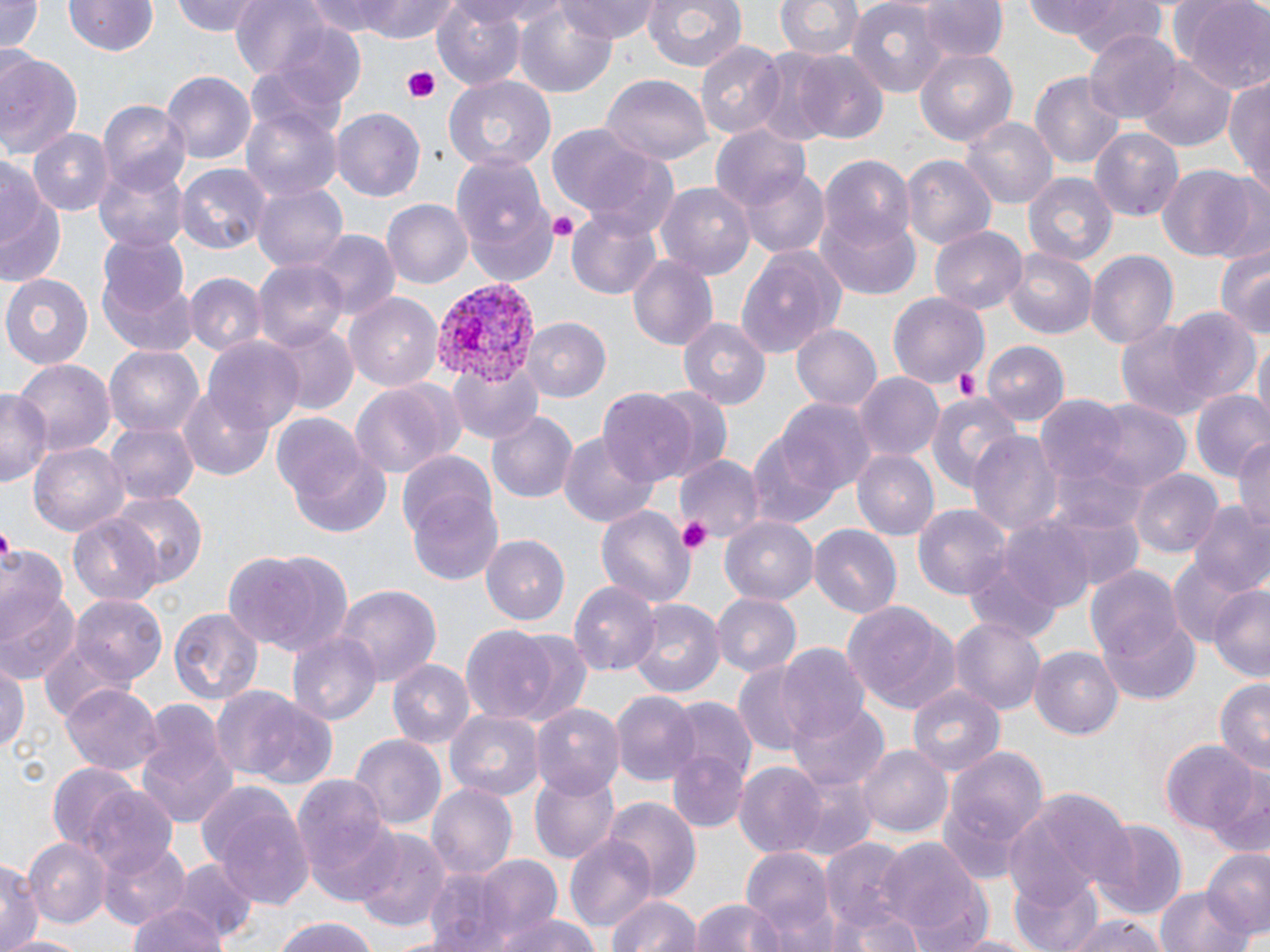

{
  "slide_level_diagnosis": "Plasmodium vivax",
  "preparation": "thin blood film",
  "platelet_locations": "approximate bounding boxes as named x1/y1/x2/y2 corners in pixels: (x1=401, y1=64, x2=444, y2=107), (x1=546, y1=211, x2=578, y2=239), (x1=951, y1=366, x2=983, y2=399), (x1=678, y1=517, x2=714, y2=556), (x1=0, y1=530, x2=17, y2=561)",
  "image_size": "1270×952 pixels",
  "field_of_view": "one of a larger specimen",
  "magnification": "1000x",
  "plasmodium_vivax_infected_red_blood_cell_locations": "approximate bounding boxes as named x1/y1/x2/y2 corners in pixels: (x1=430, y1=283, x2=538, y2=390)",
  "uninfected_red_blood_cell_locations": "approximate bounding boxes as named x1/y1/x2/y2 corners in pixels: (x1=0, y1=0, x2=43, y2=54), (x1=66, y1=0, x2=158, y2=58), (x1=172, y1=0, x2=265, y2=36), (x1=230, y1=0, x2=331, y2=79), (x1=305, y1=0, x2=402, y2=37), (x1=357, y1=0, x2=463, y2=41), (x1=430, y1=0, x2=529, y2=88), (x1=557, y1=0, x2=662, y2=42), (x1=642, y1=0, x2=748, y2=72), (x1=775, y1=0, x2=863, y2=62), (x1=847, y1=0, x2=948, y2=97), (x1=1025, y1=0, x2=1169, y2=52), (x1=1170, y1=0, x2=1270, y2=92), (x1=514, y1=1, x2=616, y2=97), (x1=917, y1=1, x2=1007, y2=64), (x1=1084, y1=28, x2=1183, y2=124), (x1=694, y1=41, x2=785, y2=143), (x1=914, y1=48, x2=1018, y2=145), (x1=0, y1=51, x2=85, y2=165), (x1=793, y1=52, x2=889, y2=144), (x1=1139, y1=60, x2=1233, y2=152), (x1=162, y1=70, x2=255, y2=162), (x1=1030, y1=71, x2=1127, y2=167), (x1=443, y1=76, x2=556, y2=173), (x1=601, y1=76, x2=711, y2=166), (x1=1226, y1=76, x2=1270, y2=188), (x1=100, y1=102, x2=193, y2=196), (x1=242, y1=102, x2=342, y2=204), (x1=331, y1=107, x2=425, y2=202), (x1=959, y1=116, x2=1057, y2=210), (x1=709, y1=123, x2=810, y2=216), (x1=545, y1=125, x2=670, y2=221), (x1=1089, y1=127, x2=1184, y2=221), (x1=27, y1=128, x2=112, y2=216), (x1=0, y1=150, x2=59, y2=275), (x1=450, y1=151, x2=557, y2=286), (x1=901, y1=155, x2=996, y2=252), (x1=820, y1=156, x2=916, y2=253), (x1=93, y1=159, x2=189, y2=249), (x1=1156, y1=163, x2=1263, y2=262), (x1=175, y1=164, x2=270, y2=256), (x1=741, y1=166, x2=831, y2=259), (x1=1024, y1=173, x2=1116, y2=264), (x1=658, y1=183, x2=755, y2=281), (x1=253, y1=184, x2=349, y2=274), (x1=383, y1=199, x2=472, y2=290), (x1=565, y1=206, x2=664, y2=300), (x1=818, y1=212, x2=921, y2=298), (x1=929, y1=225, x2=1028, y2=312), (x1=310, y1=231, x2=399, y2=321), (x1=97, y1=234, x2=191, y2=321), (x1=736, y1=246, x2=845, y2=358), (x1=1216, y1=247, x2=1270, y2=340), (x1=1005, y1=249, x2=1097, y2=340), (x1=1086, y1=250, x2=1177, y2=348), (x1=628, y1=252, x2=720, y2=351), (x1=253, y1=259, x2=349, y2=353), (x1=99, y1=271, x2=199, y2=360), (x1=2, y1=272, x2=95, y2=368), (x1=185, y1=272, x2=265, y2=357), (x1=346, y1=292, x2=444, y2=391), (x1=889, y1=293, x2=989, y2=387), (x1=1167, y1=310, x2=1260, y2=407), (x1=1113, y1=316, x2=1226, y2=419), (x1=522, y1=318, x2=611, y2=402), (x1=678, y1=318, x2=770, y2=410), (x1=262, y1=322, x2=358, y2=414), (x1=790, y1=323, x2=883, y2=412), (x1=1251, y1=336, x2=1270, y2=428), (x1=204, y1=337, x2=304, y2=435), (x1=981, y1=343, x2=1067, y2=425), (x1=104, y1=346, x2=204, y2=440), (x1=15, y1=358, x2=116, y2=459), (x1=450, y1=358, x2=545, y2=444), (x1=854, y1=373, x2=942, y2=461), (x1=350, y1=383, x2=457, y2=477), (x1=179, y1=388, x2=274, y2=480), (x1=646, y1=388, x2=734, y2=480), (x1=0, y1=389, x2=50, y2=487), (x1=597, y1=390, x2=697, y2=488), (x1=928, y1=391, x2=1025, y2=491), (x1=1191, y1=391, x2=1270, y2=486), (x1=773, y1=395, x2=876, y2=496), (x1=1033, y1=396, x2=1135, y2=488), (x1=1074, y1=397, x2=1194, y2=493), (x1=485, y1=409, x2=578, y2=506), (x1=273, y1=413, x2=370, y2=508), (x1=106, y1=421, x2=196, y2=505), (x1=557, y1=430, x2=660, y2=529), (x1=745, y1=430, x2=842, y2=531), (x1=968, y1=430, x2=1061, y2=536), (x1=1234, y1=435, x2=1270, y2=537), (x1=29, y1=443, x2=128, y2=536), (x1=851, y1=450, x2=938, y2=541), (x1=291, y1=451, x2=396, y2=539), (x1=678, y1=455, x2=762, y2=543), (x1=1134, y1=469, x2=1222, y2=559), (x1=405, y1=485, x2=504, y2=589), (x1=106, y1=492, x2=207, y2=586), (x1=1191, y1=503, x2=1270, y2=597), (x1=596, y1=505, x2=692, y2=607), (x1=915, y1=505, x2=1010, y2=603), (x1=1040, y1=506, x2=1148, y2=592), (x1=69, y1=513, x2=165, y2=604), (x1=720, y1=517, x2=817, y2=604), (x1=808, y1=523, x2=902, y2=618), (x1=486, y1=535, x2=569, y2=625), (x1=0, y1=542, x2=70, y2=640), (x1=222, y1=546, x2=352, y2=656), (x1=1167, y1=555, x2=1260, y2=648), (x1=1083, y1=563, x2=1185, y2=669), (x1=569, y1=578, x2=657, y2=676), (x1=1208, y1=582, x2=1270, y2=682), (x1=333, y1=583, x2=441, y2=683), (x1=0, y1=592, x2=80, y2=682), (x1=709, y1=593, x2=800, y2=678), (x1=71, y1=597, x2=168, y2=689), (x1=627, y1=599, x2=724, y2=699), (x1=842, y1=601, x2=962, y2=712), (x1=167, y1=605, x2=263, y2=707), (x1=1101, y1=617, x2=1200, y2=705), (x1=949, y1=618, x2=1047, y2=715), (x1=459, y1=624, x2=565, y2=728), (x1=289, y1=631, x2=379, y2=725), (x1=41, y1=639, x2=129, y2=722), (x1=775, y1=645, x2=870, y2=742), (x1=1029, y1=645, x2=1123, y2=738), (x1=388, y1=659, x2=474, y2=753), (x1=731, y1=659, x2=823, y2=756), (x1=0, y1=661, x2=28, y2=760), (x1=1214, y1=678, x2=1270, y2=774), (x1=906, y1=682, x2=1007, y2=775), (x1=61, y1=684, x2=164, y2=775), (x1=211, y1=687, x2=338, y2=791), (x1=613, y1=692, x2=699, y2=787), (x1=665, y1=698, x2=756, y2=799), (x1=786, y1=701, x2=887, y2=791), (x1=135, y1=702, x2=236, y2=831), (x1=531, y1=702, x2=624, y2=798), (x1=448, y1=711, x2=543, y2=801), (x1=349, y1=733, x2=447, y2=835), (x1=1164, y1=741, x2=1260, y2=835), (x1=859, y1=743, x2=951, y2=838), (x1=936, y1=743, x2=1051, y2=881), (x1=666, y1=746, x2=751, y2=835), (x1=47, y1=763, x2=140, y2=852), (x1=733, y1=764, x2=826, y2=855), (x1=529, y1=765, x2=620, y2=865), (x1=788, y1=771, x2=878, y2=861), (x1=290, y1=772, x2=396, y2=893), (x1=1209, y1=775, x2=1270, y2=860), (x1=425, y1=783, x2=517, y2=882), (x1=200, y1=785, x2=314, y2=910), (x1=1012, y1=787, x2=1136, y2=904), (x1=82, y1=788, x2=180, y2=880), (x1=605, y1=797, x2=699, y2=901), (x1=1088, y1=819, x2=1189, y2=921), (x1=354, y1=829, x2=450, y2=931), (x1=564, y1=835, x2=657, y2=935), (x1=25, y1=837, x2=111, y2=928), (x1=877, y1=838, x2=988, y2=945), (x1=819, y1=839, x2=913, y2=931), (x1=100, y1=841, x2=191, y2=928), (x1=740, y1=847, x2=835, y2=945), (x1=1201, y1=851, x2=1270, y2=940), (x1=2, y1=856, x2=44, y2=952), (x1=473, y1=856, x2=562, y2=945), (x1=168, y1=858, x2=260, y2=944), (x1=421, y1=867, x2=521, y2=952), (x1=1009, y1=873, x2=1106, y2=952), (x1=1152, y1=883, x2=1253, y2=952), (x1=606, y1=893, x2=700, y2=952), (x1=690, y1=896, x2=789, y2=952), (x1=833, y1=902, x2=930, y2=952), (x1=125, y1=904, x2=232, y2=952), (x1=492, y1=914, x2=607, y2=952), (x1=1063, y1=915, x2=1170, y2=952), (x1=269, y1=916, x2=381, y2=952), (x1=942, y1=931, x2=1048, y2=951), (x1=5, y1=934, x2=89, y2=952)",
  "stain": "May-Grünwald-Giemsa",
  "modality": "optical microscopy"
}